Classify this cell by malaria status.
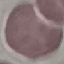
It is uninfected.

stain: Giemsa
image_type: automatically extracted cell patch, resized to 64 × 64 pixels
preparation: thin blood film
capture: smartphone through the microscope eyepiece